Identify the parasite.
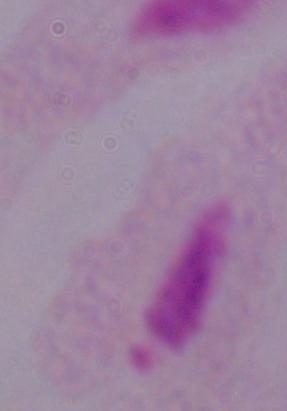
This is a trichomonad.

Summary:
  - Modality: photomicrograph
  - Magnification: 1000x